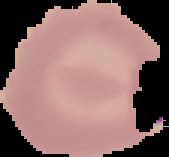
malaria status = parasitized
image type = segmented cell region with the area outside set to black
image size = 169×157 pixels
preparation = thin blood smear